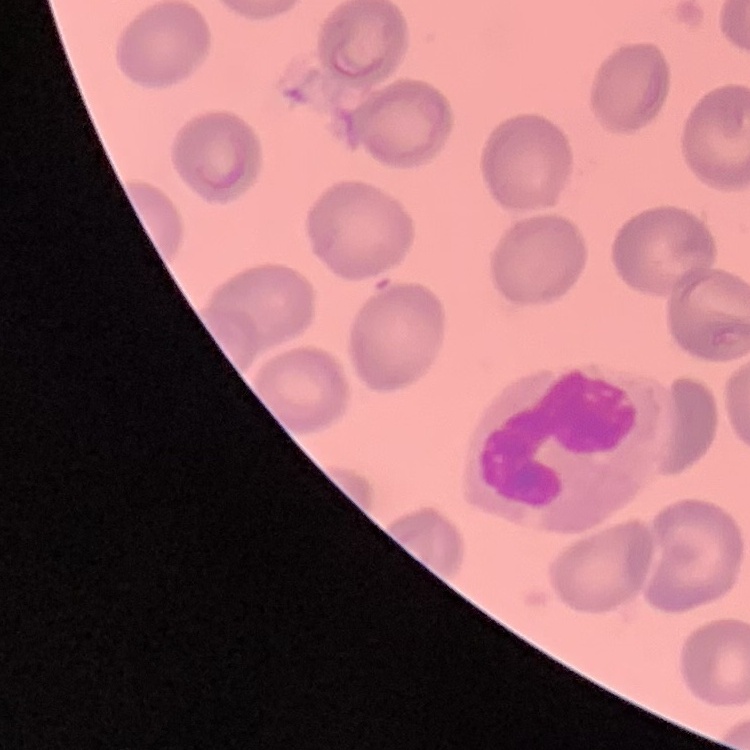

The red blood cells exhibit no rouleaux formation. Stained with either Field's or Giemsa. Thin peripheral smear. Square crop of a larger photomicrograph.